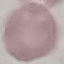

Summary:
  - Result: no malaria parasites detected
  - Image type: automatically extracted cell patch, resized to 64 × 64 pixels
  - Preparation: thin blood film
  - Stain: Giemsa
  - Capture: smartphone camera at the microscope eyepiece